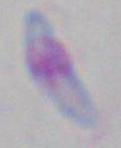
Summary:
  - Magnification: 1000x
  - Identification: Toxoplasma gondii
  - Modality: micrograph